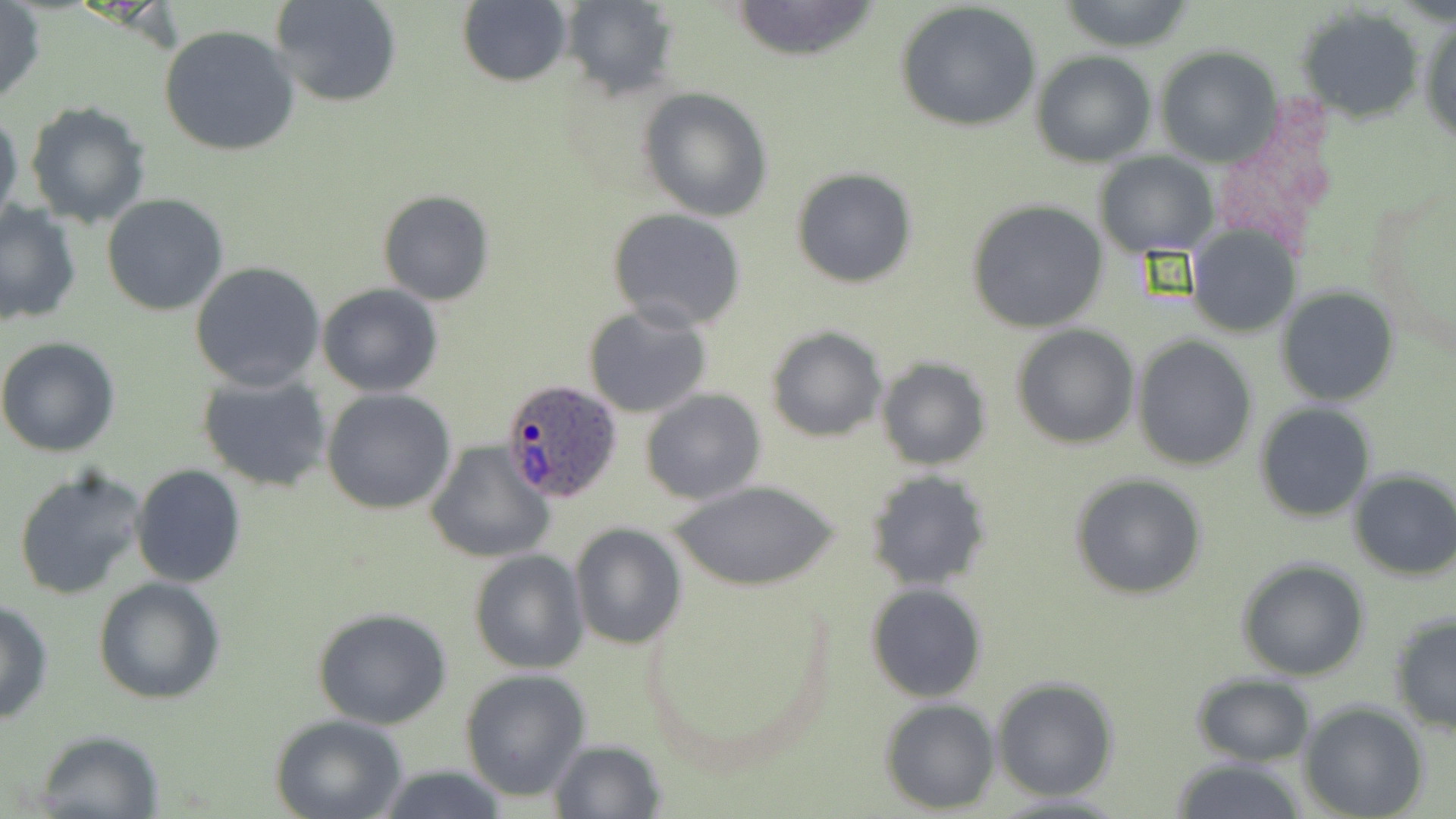
Summary:
  - Coordinate format: approximate bounding boxes as [x1, y1, x2, y2] in pixels
  - Plasmodium ovale-infected red blood cell locations: [503, 378, 625, 502]
  - Uninfected red blood cell locations: [270, 0, 403, 107], [729, 0, 884, 61], [557, 1, 679, 99], [1057, 1, 1196, 51], [0, 2, 46, 107], [457, 2, 572, 87], [896, 3, 1043, 134], [1296, 9, 1422, 122], [1420, 16, 1456, 147], [158, 24, 299, 157], [1155, 47, 1281, 166], [1032, 52, 1156, 167], [638, 87, 773, 221], [24, 100, 151, 229], [0, 111, 23, 232], [1092, 151, 1217, 257], [791, 168, 917, 287], [377, 190, 494, 306], [102, 193, 229, 316], [966, 198, 1108, 333], [0, 202, 82, 326], [605, 209, 749, 333], [1186, 226, 1300, 337], [191, 262, 325, 392], [317, 282, 444, 396], [1277, 288, 1398, 407], [581, 304, 713, 418], [1012, 324, 1140, 449], [765, 326, 888, 443], [1131, 335, 1259, 471], [0, 337, 121, 457], [874, 357, 991, 469], [197, 373, 334, 493], [323, 389, 456, 514], [640, 389, 768, 506], [1255, 403, 1374, 521], [426, 440, 555, 564], [131, 463, 246, 587], [12, 464, 147, 601], [1348, 468, 1456, 581], [866, 469, 993, 592], [1069, 473, 1208, 599], [671, 479, 841, 592], [569, 525, 686, 649], [469, 550, 589, 674], [1235, 558, 1371, 681], [92, 577, 227, 705], [867, 583, 987, 702], [643, 585, 837, 775], [0, 597, 54, 726], [311, 606, 453, 730], [1388, 613, 1456, 739], [459, 669, 590, 801], [1192, 673, 1316, 767], [990, 676, 1120, 801], [880, 699, 1000, 813], [1301, 702, 1429, 819], [271, 715, 408, 819], [33, 729, 165, 817], [547, 738, 666, 816], [1165, 758, 1313, 819], [371, 765, 514, 819]
  - Slide-level diagnosis: Plasmodium ovale
  - Modality: light microscopy
  - Field of view: one of a larger specimen
  - Stain: May-Grünwald-Giemsa
  - Preparation: thin blood film
  - Image size: 1456×819 pixels
  - Magnification: 1000x